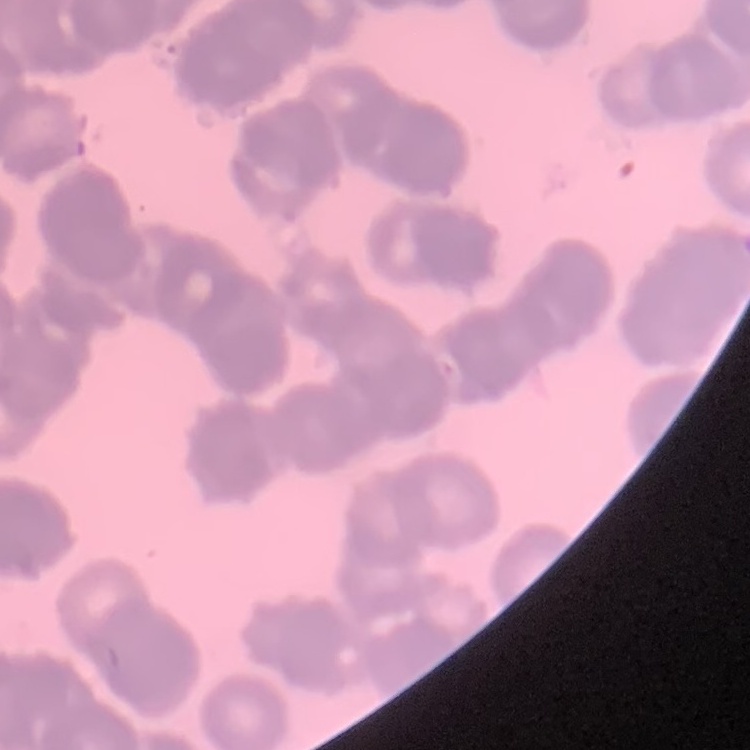
Summary:
  - Erythrocyte morphology: rouleaux formation
  - Image type: one tile cut from a larger photomicrograph
  - Stain: Field's or Giemsa
  - Preparation: thin peripheral smear